Give the extent of all Plasmodium ovale-infected red blood cells.
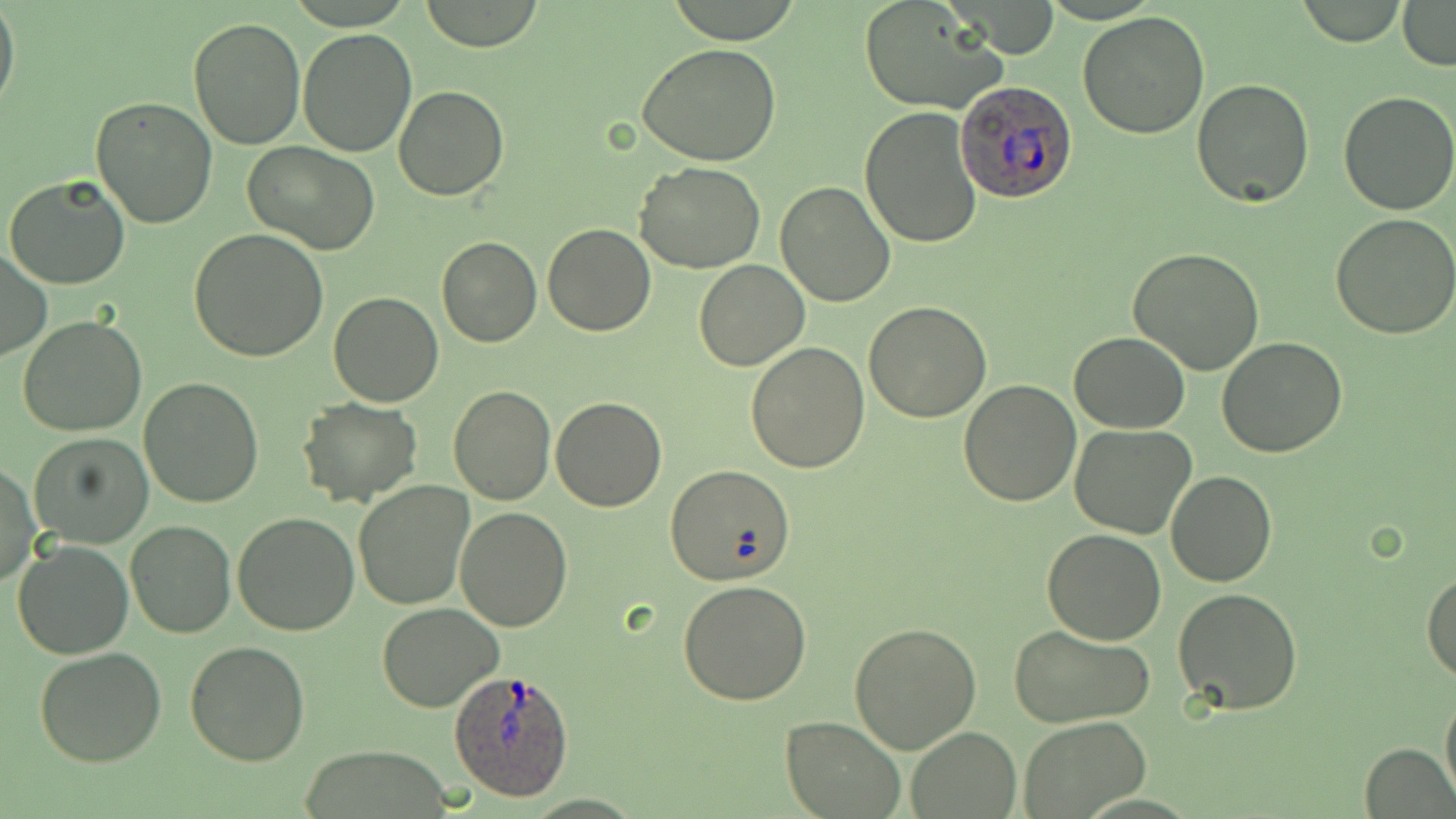
Approximate bounding boxes as [x1, y1, x2, y2] in pixels.
Plasmodium ovale-infected red blood cells: [956, 79, 1078, 206], [446, 667, 578, 802].

Uninfected red blood cell locations: [418, 0, 548, 51], [664, 0, 806, 45], [1296, 1, 1406, 46], [1398, 1, 1456, 69], [0, 2, 20, 117], [858, 2, 1009, 114], [1077, 11, 1209, 138], [188, 18, 307, 152], [297, 29, 417, 157], [637, 43, 781, 166], [1191, 78, 1313, 208], [394, 85, 508, 200], [1339, 92, 1455, 214], [91, 96, 218, 228], [860, 105, 982, 249], [244, 142, 381, 256], [635, 161, 765, 273], [4, 175, 132, 291], [775, 182, 896, 306], [1331, 212, 1456, 339], [543, 222, 656, 337], [188, 228, 331, 362], [437, 235, 542, 348], [1127, 247, 1266, 375], [0, 251, 50, 362], [693, 259, 809, 371], [328, 292, 445, 407], [864, 302, 991, 422], [18, 316, 149, 438], [1068, 332, 1192, 433], [1217, 338, 1349, 458], [747, 342, 870, 472], [139, 376, 267, 508], [956, 379, 1082, 506], [447, 385, 556, 505], [550, 395, 667, 512], [296, 398, 422, 507], [1068, 423, 1197, 539], [27, 432, 156, 549], [0, 464, 41, 590], [666, 464, 796, 586], [1167, 470, 1278, 587], [352, 479, 474, 610], [457, 506, 572, 629], [233, 512, 359, 636], [126, 519, 236, 637], [1043, 528, 1166, 645], [11, 541, 134, 659], [1423, 571, 1456, 684], [678, 579, 811, 703], [1172, 589, 1304, 714], [377, 603, 504, 712], [850, 623, 981, 753], [1009, 624, 1157, 728], [185, 641, 310, 767], [33, 647, 167, 768], [1439, 686, 1456, 808], [781, 714, 905, 818], [1016, 717, 1149, 817], [906, 727, 1021, 817], [1358, 741, 1454, 818]. Slide-level diagnosis: Plasmodium ovale. May-Grünwald-Giemsa-stained preparation. Light microscopy. One field of a larger specimen. 1000x magnification. Image is 1456×819 pixels. Thin blood film.